State which parasite is depicted.
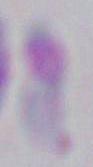
This is Toxoplasma gondii.

Summary:
  - Magnification: 1000x
  - Modality: photomicrograph